Assess the morphology of the erythrocytes.
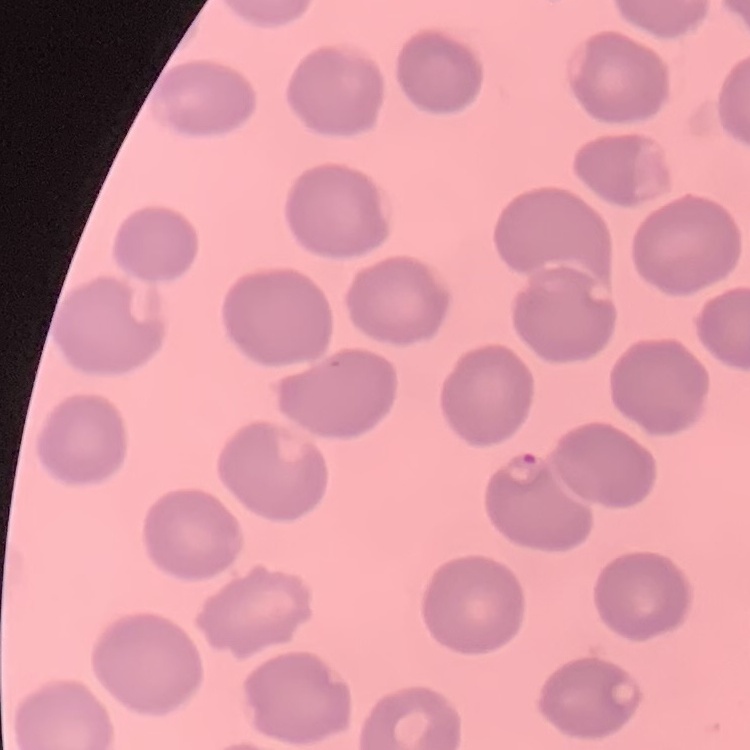
They show no rouleaux formation.

stain = Field's or Giemsa
preparation = thin blood film
image type = square crop of a larger photomicrograph